Look for Plasmodium parasites.
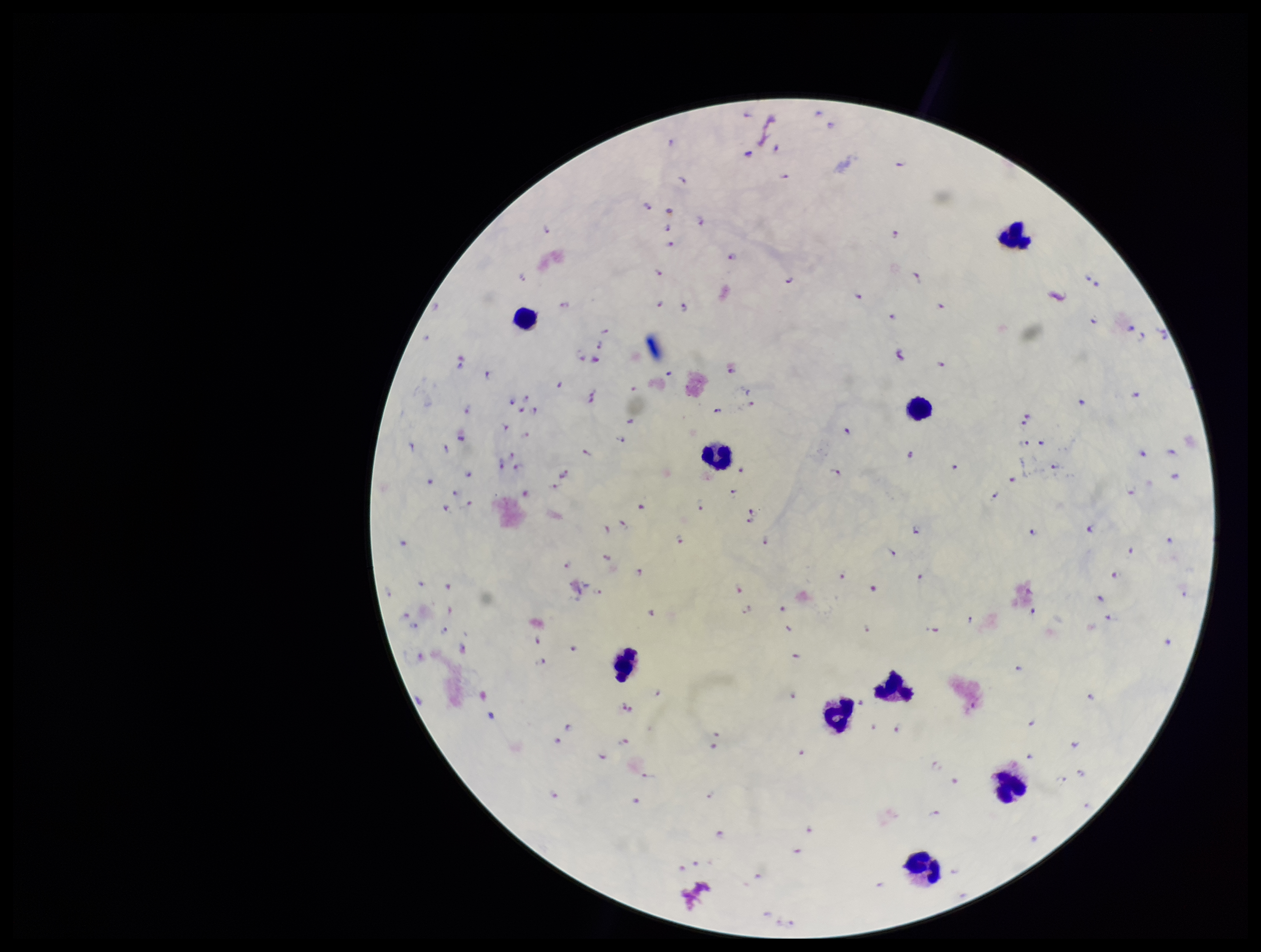
Detected.

Species reported for this patient: Plasmodium falciparum. Parasite count: 170. Stained with Giemsa. Image is 1261×952 pixels. Patient malaria status: infected. One field from this slide. Preparation: thick blood smear. Leukocyte count: 9. Photographed through the microscope eyepiece with a smartphone camera.